Assess this cell for malaria.
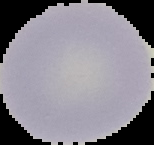
It is uninfected.

image size = 154×145 pixels
preparation = thin blood smear
image type = segmented cell region with the area outside set to black